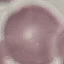

Summary:
  - Malaria status: uninfected
  - Stain: Giemsa
  - Capture: smartphone camera at the microscope eyepiece
  - Image type: automatically extracted cell patch, resized to 64 × 64 pixels
  - Preparation: thin blood smear